State which cell type is depicted.
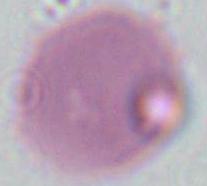
An erythrocyte.

Captured at 1000x magnification. Micrograph.